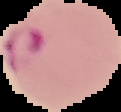
Summary:
  - Image size: 121×112 pixels
  - Image type: segmented cell region on a black background
  - Preparation: thin blood smear
  - Result: malaria parasites detected